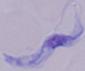

Summary:
  - Magnification: 1000x
  - Identification: trypanosome
  - Modality: photomicrograph